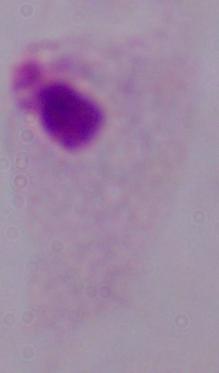

{
  "identification": "trichomonad",
  "modality": "micrograph",
  "magnification": "1000x"
}